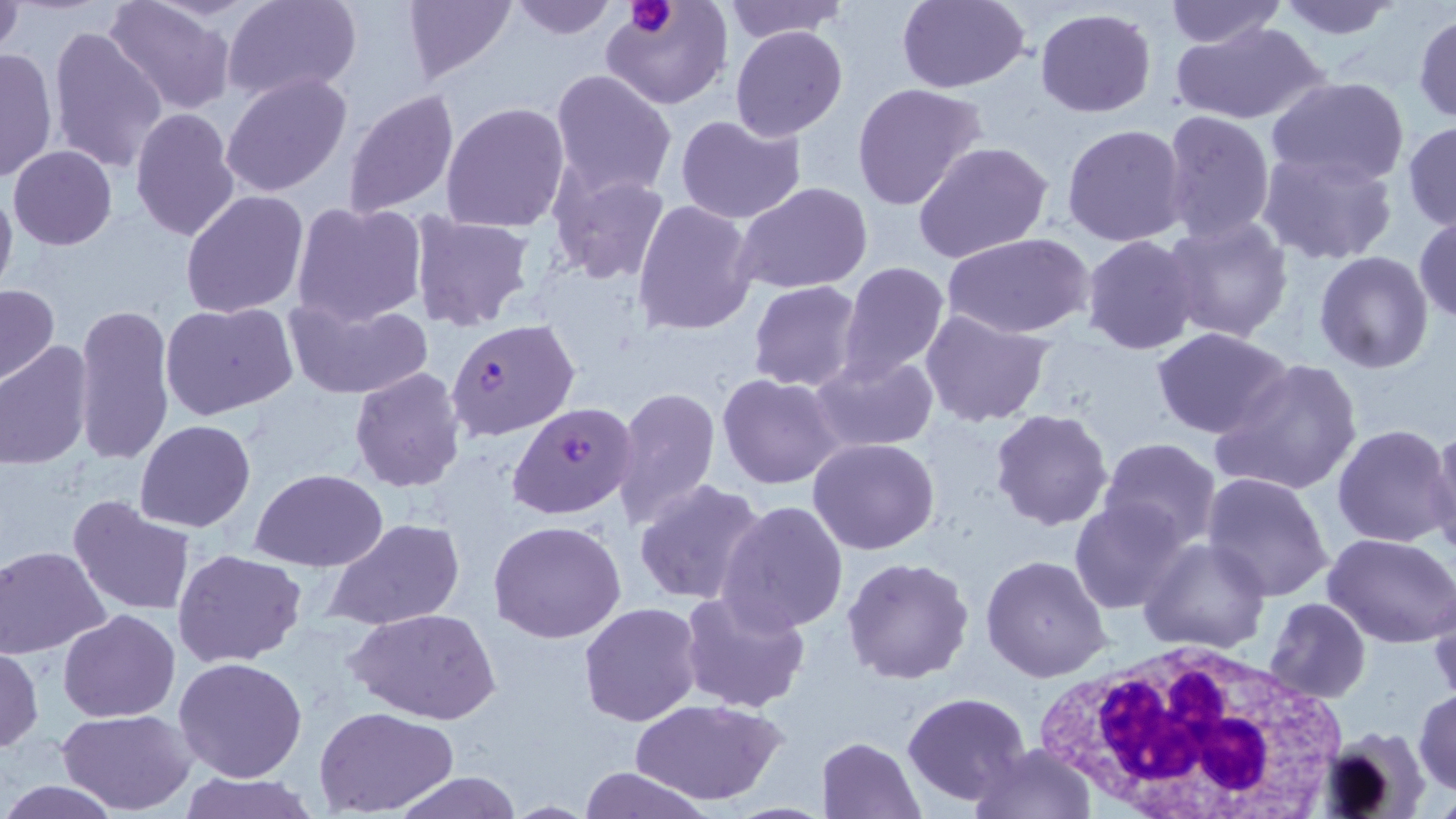
slide_level_diagnosis: Plasmodium falciparum
modality: optical microscopy
image_size: 1456×819 pixels
white_blood_cell_locations: 'approximate bounding boxes as [x1, y1, x2, y2] in pixels: [1033, 638, 1353, 817]'
preparation: thin blood smear
magnification: 1000x
stain: May-Grünwald-Giemsa
field_of_view: single
uninfected_red_blood_cell_locations: 'approximate bounding boxes as [x1, y1, x2, y2] in pixels: [104, 0, 235, 115], [222, 0, 364, 104], [400, 0, 518, 85], [507, 0, 616, 41], [720, 0, 850, 43], [893, 0, 1031, 92], [1272, 0, 1403, 39], [601, 1, 732, 111], [1165, 1, 1284, 50], [1, 2, 26, 63], [1034, 7, 1157, 116], [1412, 11, 1456, 124], [1169, 20, 1330, 126], [47, 24, 169, 176], [730, 25, 849, 142], [699, 41, 836, 194], [0, 45, 59, 185], [549, 70, 677, 198], [221, 72, 352, 197], [1267, 75, 1409, 187], [851, 82, 987, 211], [341, 88, 460, 218], [440, 100, 570, 233], [130, 107, 242, 244], [1160, 109, 1276, 244], [675, 114, 806, 223], [1402, 121, 1456, 232], [1061, 124, 1188, 247], [913, 141, 1055, 266], [8, 145, 118, 249], [1257, 149, 1400, 267], [548, 166, 673, 284], [0, 181, 17, 304], [735, 182, 874, 294], [181, 189, 309, 318], [631, 198, 761, 337], [291, 199, 428, 327], [408, 212, 535, 334], [1414, 214, 1455, 326], [1161, 216, 1294, 342], [942, 232, 1095, 340], [1080, 236, 1199, 355], [1315, 251, 1434, 373], [837, 261, 950, 382], [747, 280, 864, 392], [0, 283, 59, 386], [284, 295, 434, 401], [160, 302, 297, 421], [72, 303, 175, 466], [919, 309, 1056, 427], [1154, 329, 1293, 439], [0, 342, 92, 470], [809, 351, 939, 454], [1209, 356, 1364, 497], [349, 367, 466, 494], [717, 374, 842, 490], [613, 385, 723, 529], [989, 409, 1113, 531], [135, 419, 255, 533], [1426, 421, 1456, 555], [1332, 424, 1454, 549], [1099, 437, 1221, 551], [808, 438, 940, 555], [250, 469, 389, 571], [1201, 473, 1333, 603], [633, 479, 767, 606], [68, 494, 197, 617], [718, 498, 849, 636], [1069, 501, 1188, 616], [323, 518, 466, 632], [488, 520, 626, 643], [1324, 531, 1456, 646], [1140, 537, 1273, 655], [3, 545, 112, 659], [173, 547, 307, 668], [981, 555, 1112, 681], [842, 556, 974, 684], [1428, 582, 1456, 706], [679, 589, 808, 714], [1264, 599, 1370, 704], [579, 602, 703, 726], [345, 608, 501, 724], [59, 610, 180, 724], [0, 645, 44, 753], [173, 657, 307, 782], [1413, 689, 1456, 796], [903, 692, 1031, 807], [631, 697, 784, 805], [315, 707, 459, 815], [57, 708, 195, 815], [1315, 729, 1434, 817], [817, 737, 926, 819], [970, 742, 1095, 819], [575, 766, 711, 819], [391, 771, 524, 818], [172, 773, 322, 819], [1, 777, 121, 818]'
plasmodium_falciparum_infected_red_blood_cell_locations: 'approximate bounding boxes as [x1, y1, x2, y2] in pixels: [446, 316, 579, 442], [506, 403, 638, 520]'
platelet_locations: 'approximate bounding boxes as [x1, y1, x2, y2] in pixels: [627, 0, 676, 38]'